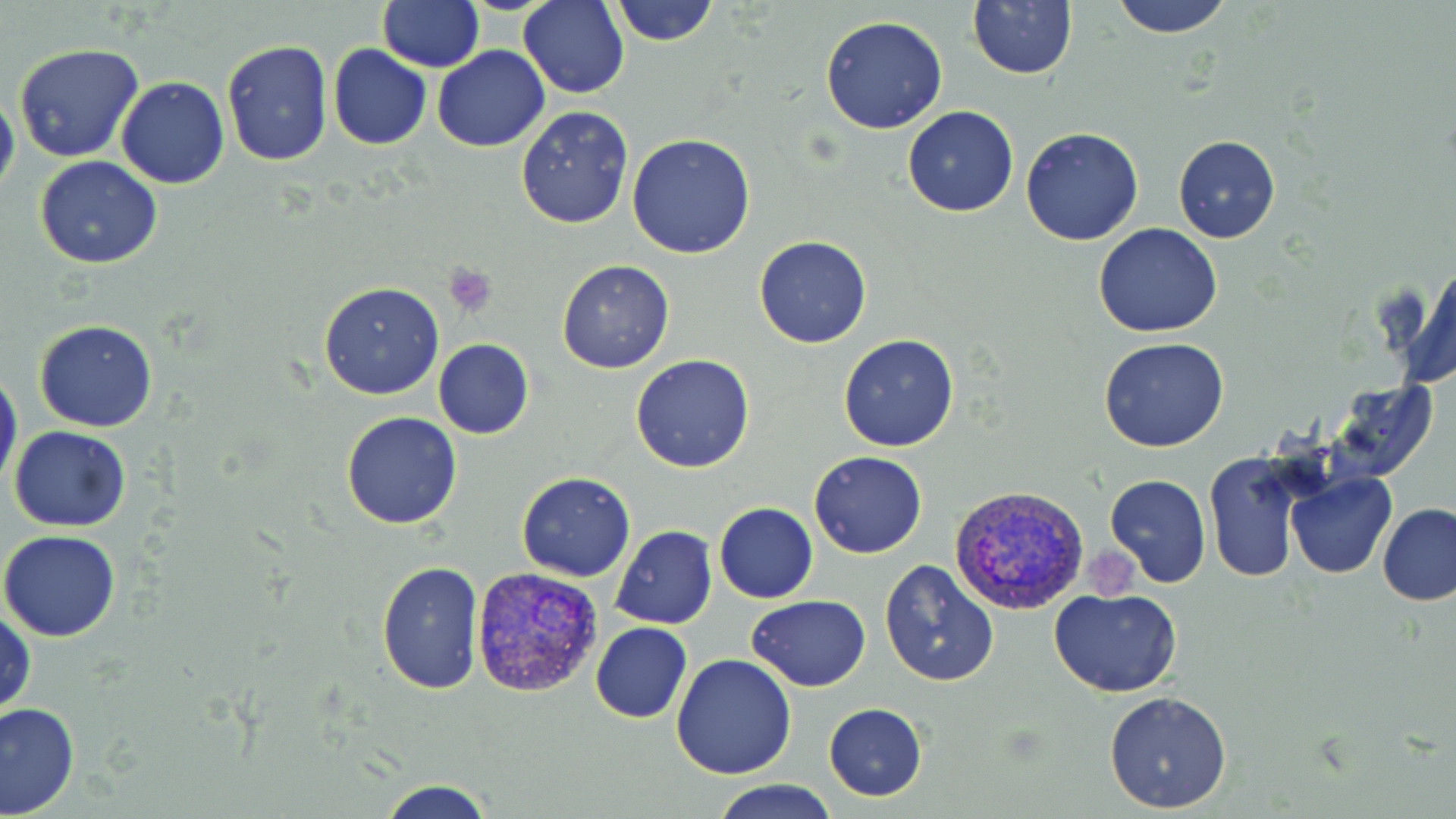
slide-level diagnosis = Plasmodium vivax
uninfected red blood cell locations = approximate bounding boxes as [x1, y1, x2, y2] in pixels: [377, 0, 483, 72], [520, 0, 630, 99], [608, 0, 722, 47], [967, 0, 1078, 79], [1109, 0, 1236, 39], [820, 16, 948, 135], [220, 40, 334, 167], [328, 43, 432, 149], [13, 44, 145, 164], [433, 44, 550, 153], [116, 76, 230, 189], [0, 90, 19, 201], [902, 105, 1018, 217], [516, 106, 633, 229], [1021, 126, 1143, 246], [627, 133, 757, 259], [1172, 136, 1281, 244], [35, 156, 163, 270], [1093, 223, 1223, 337], [755, 236, 872, 349], [556, 259, 675, 374], [1406, 264, 1456, 389], [318, 280, 446, 401], [34, 319, 157, 432], [839, 334, 960, 452], [1099, 337, 1231, 453], [433, 339, 533, 440], [630, 354, 757, 474], [0, 366, 22, 491], [1322, 379, 1437, 484], [341, 411, 463, 529], [8, 426, 131, 531], [809, 451, 927, 558], [1205, 453, 1305, 583], [516, 470, 635, 582], [1286, 471, 1395, 578], [1104, 473, 1212, 587], [714, 501, 819, 602], [1378, 503, 1456, 605], [610, 526, 718, 629], [1, 529, 122, 643], [878, 559, 998, 686], [376, 560, 484, 694], [1050, 588, 1182, 697], [748, 595, 872, 690], [0, 602, 35, 721], [590, 621, 693, 722], [672, 654, 797, 778], [1103, 690, 1233, 813], [0, 701, 80, 817], [824, 703, 928, 800], [374, 779, 499, 819], [713, 779, 836, 819]
image size = 1456×819 pixels
magnification = 1000x
platelet locations = approximate bounding boxes as [x1, y1, x2, y2] in pixels: [443, 264, 494, 316]
stain = May-Grünwald-Giemsa
modality = optical microscopy
Plasmodium vivax-infected red blood cell locations = approximate bounding boxes as [x1, y1, x2, y2] in pixels: [951, 484, 1090, 615], [470, 565, 605, 697]
field of view = single
preparation = thin blood film